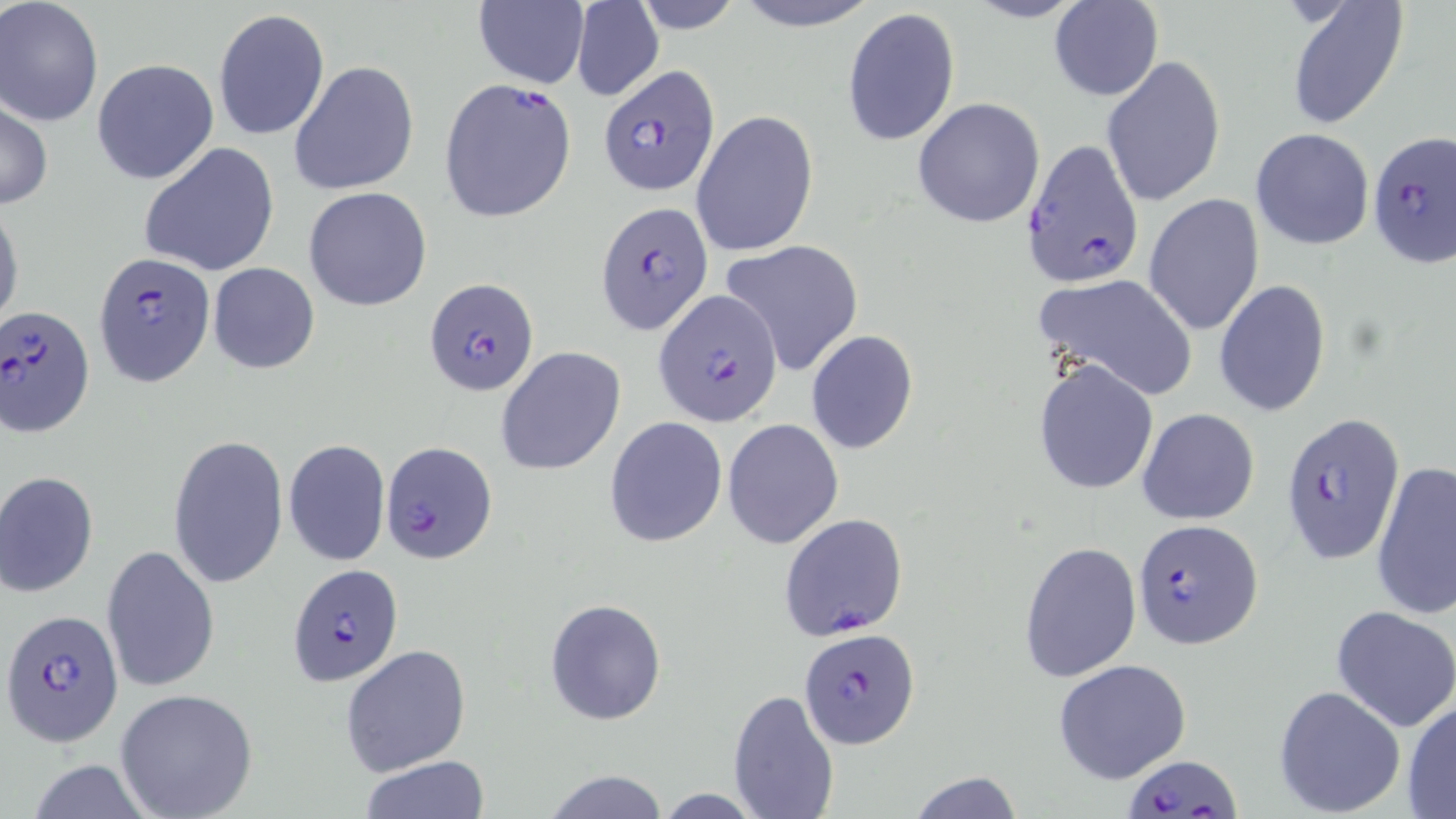 Approximate bounding boxes as [x1, y1, x2, y2] in pixels. Plasmodium falciparum-infected red blood cell locations: [597, 64, 722, 196], [439, 79, 578, 223], [1368, 133, 1455, 268], [1019, 137, 1142, 288], [595, 201, 714, 337], [93, 250, 216, 388], [424, 277, 541, 396], [653, 291, 784, 427], [1, 306, 96, 436], [1279, 412, 1405, 565], [380, 439, 498, 565], [777, 512, 909, 640], [1132, 519, 1263, 650], [287, 564, 404, 684], [3, 612, 122, 745], [795, 627, 913, 749], [1127, 752, 1239, 818]. Uninfected red blood cell locations: [631, 0, 749, 32], [728, 0, 883, 31], [964, 0, 1090, 24], [0, 1, 104, 126], [1049, 1, 1162, 101], [472, 2, 589, 88], [1284, 2, 1409, 129], [570, 4, 664, 101], [842, 8, 960, 146], [211, 9, 330, 142], [1100, 54, 1224, 207], [91, 58, 218, 186], [290, 62, 420, 196], [913, 97, 1045, 229], [0, 99, 51, 210], [691, 109, 819, 259], [1251, 127, 1374, 250], [139, 143, 279, 276], [304, 186, 432, 311], [1144, 194, 1265, 337], [0, 201, 23, 334], [719, 239, 864, 376], [207, 263, 320, 373], [1035, 274, 1198, 401], [1213, 281, 1332, 416], [805, 330, 918, 455], [495, 347, 626, 475], [1032, 356, 1159, 496], [1137, 408, 1260, 525], [603, 416, 727, 547], [723, 418, 844, 549], [168, 434, 288, 590], [283, 439, 390, 567], [1372, 461, 1456, 621], [0, 471, 100, 597], [1019, 541, 1143, 683], [103, 543, 219, 695], [545, 599, 667, 725], [1331, 605, 1456, 733], [340, 643, 473, 776], [1052, 659, 1192, 783], [1272, 684, 1405, 817], [115, 688, 260, 819], [727, 688, 840, 819], [1403, 698, 1456, 817], [357, 757, 494, 817], [22, 759, 157, 819], [539, 770, 673, 818], [905, 772, 1024, 818]. Slide-level diagnosis: Plasmodium falciparum. May-Grünwald-Giemsa stain. Image is 1456×819 pixels. One field of a larger specimen. Light microscopy. Captured at 1000x magnification. Thin blood smear.